Point out each malaria parasite and classify it by life-cycle stage.
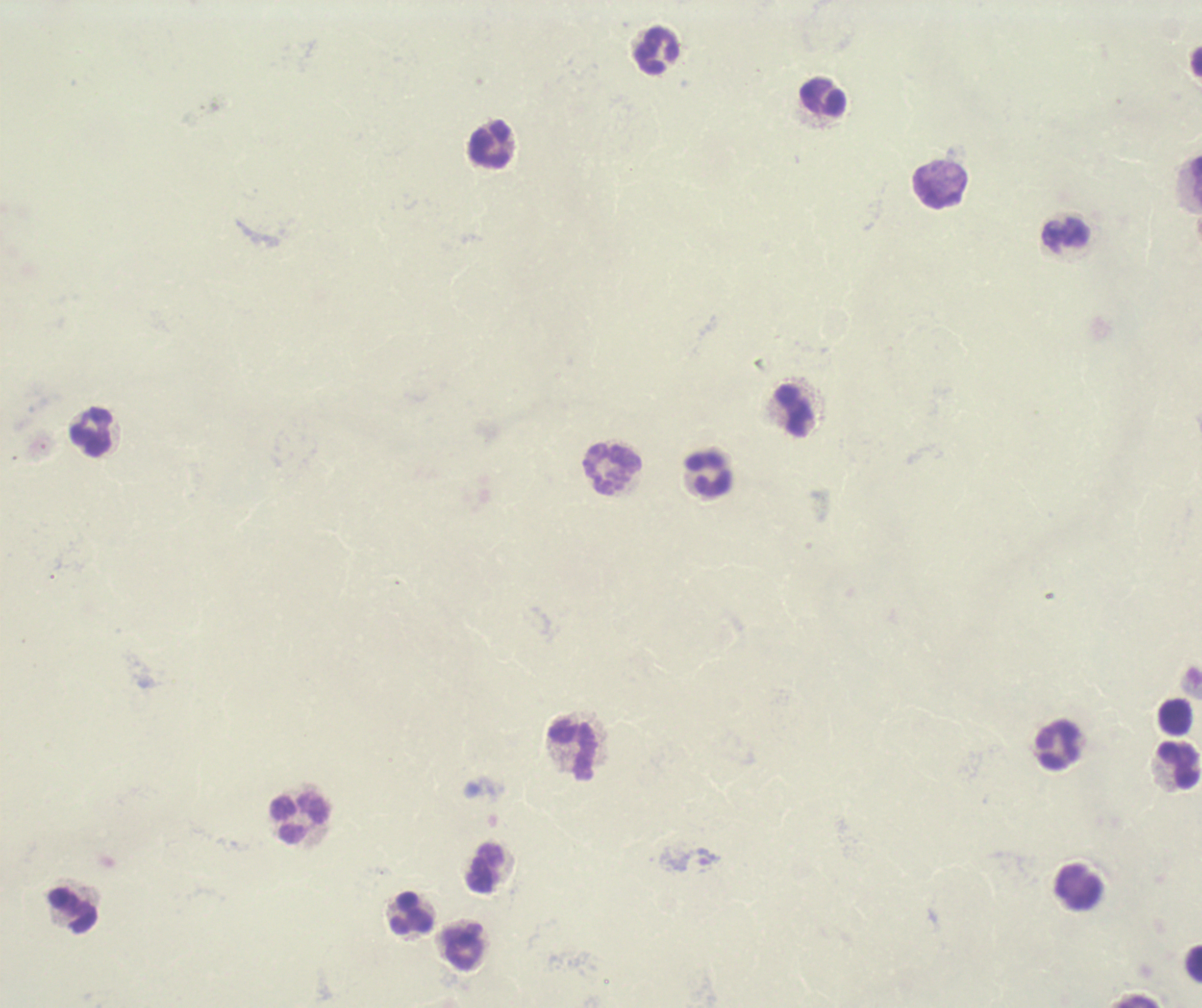
Negative for malaria parasites.

Approximate centers as {x, y} in pixels.
Summary:
  - Leukocyte locations: {658, 52}, {823, 99}, {491, 145}, {942, 186}, {1067, 236}, {795, 412}, {92, 432}, {613, 471}, {710, 476}, {1176, 718}, {1058, 745}, {571, 753}, {1181, 766}, {300, 819}, {486, 870}, {1078, 885}, {74, 911}, {414, 915}, {465, 947}, {1194, 965}
  - Background quality: unsatisfactory
  - Preparation: thick smear of blood
  - Field of view: one from this slide
  - Context: previously used in a real diagnosis
  - Magnification: 100x
  - Stain: Romanowsky
  - Image size: 1202×1008 pixels